Assess this cell for malaria.
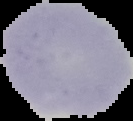

Uninfected.

From a thin blood film. Image is 133×121 pixels. Segmented cell region on a black background.